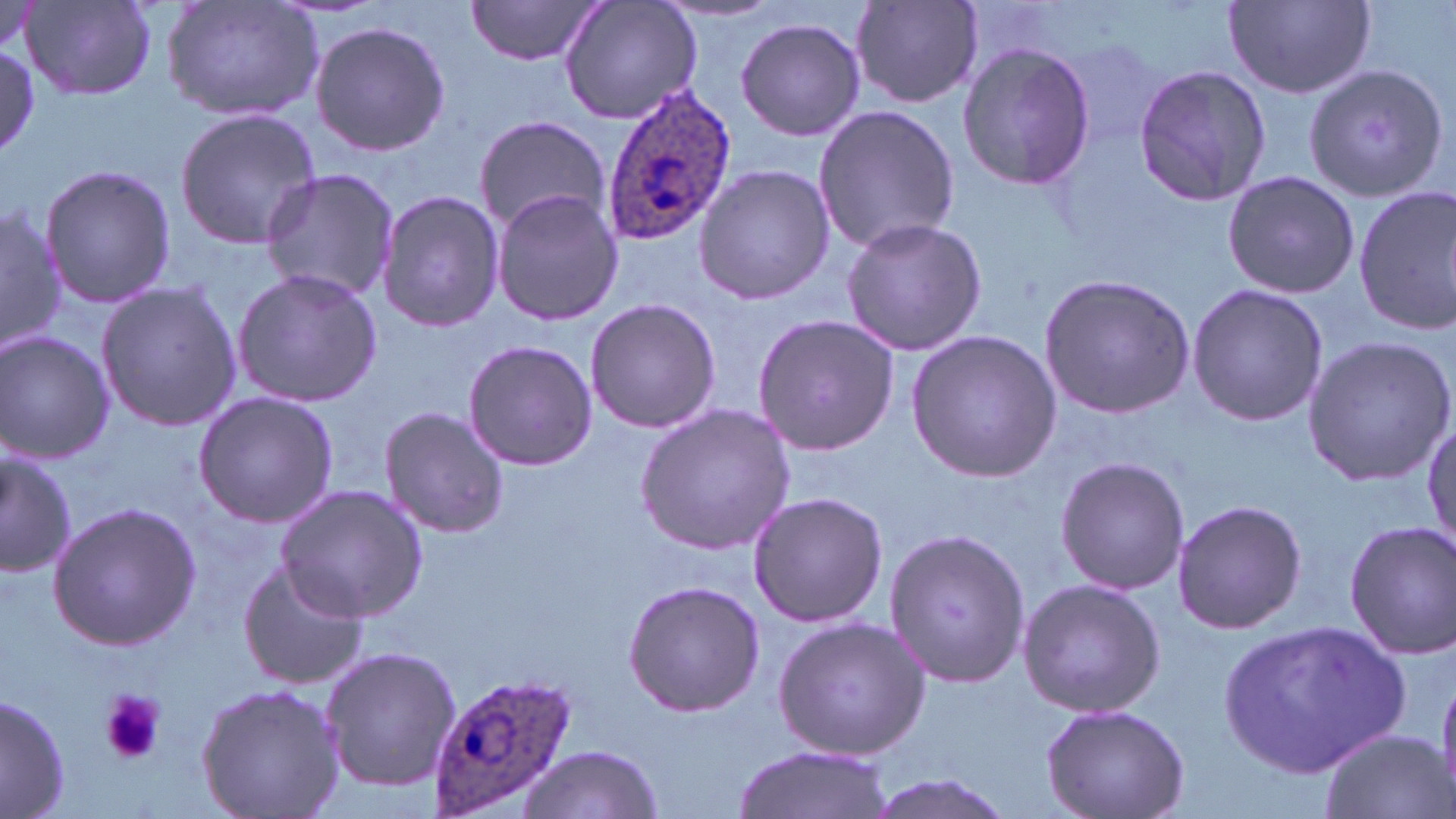
Summary:
  - Coordinate format: approximate bounding boxes as [x1, y1, x2, y2] in pixels
  - Plasmodium ovale-infected red blood cell locations: [597, 83, 738, 243], [427, 670, 579, 814]
  - Uninfected red blood cell locations: [463, 0, 609, 68], [557, 0, 704, 126], [1223, 0, 1377, 98], [21, 1, 157, 101], [161, 1, 323, 122], [850, 1, 985, 109], [734, 18, 865, 140], [309, 20, 449, 157], [0, 43, 40, 159], [957, 43, 1097, 189], [1133, 62, 1273, 208], [1305, 62, 1451, 205], [812, 104, 960, 256], [174, 108, 321, 251], [472, 114, 610, 236], [39, 163, 174, 308], [693, 163, 836, 306], [259, 168, 401, 304], [1221, 170, 1360, 298], [1353, 186, 1456, 335], [490, 188, 624, 325], [376, 192, 505, 333], [0, 199, 65, 357], [839, 216, 988, 357], [231, 268, 382, 408], [1037, 270, 1195, 419], [96, 281, 242, 431], [1186, 282, 1328, 427], [583, 296, 721, 433], [753, 314, 898, 454], [906, 329, 1064, 484], [0, 331, 115, 464], [1300, 334, 1454, 487], [462, 339, 598, 470], [193, 391, 338, 526], [635, 403, 797, 554], [379, 407, 511, 538], [1423, 421, 1454, 558], [0, 448, 76, 574], [1054, 456, 1189, 596], [276, 487, 426, 622], [746, 491, 887, 628], [1171, 497, 1307, 636], [47, 502, 200, 650], [1344, 522, 1455, 658], [882, 525, 1029, 690], [235, 559, 369, 690], [1016, 577, 1167, 719], [623, 580, 766, 718], [772, 617, 930, 761], [1223, 620, 1414, 776], [320, 645, 462, 790], [195, 683, 345, 819], [1, 692, 70, 819], [1041, 701, 1191, 819], [1317, 729, 1450, 819], [731, 740, 892, 819], [517, 745, 664, 818], [862, 773, 1013, 819]
  - Platelet locations: [99, 688, 164, 766]
  - Slide-level diagnosis: Plasmodium ovale
  - Stain: May-Grünwald-Giemsa
  - Magnification: 1000x
  - Field of view: single
  - Image size: 1456×819 pixels
  - Preparation: thin blood smear
  - Modality: optical microscopy